Give the preparation type.
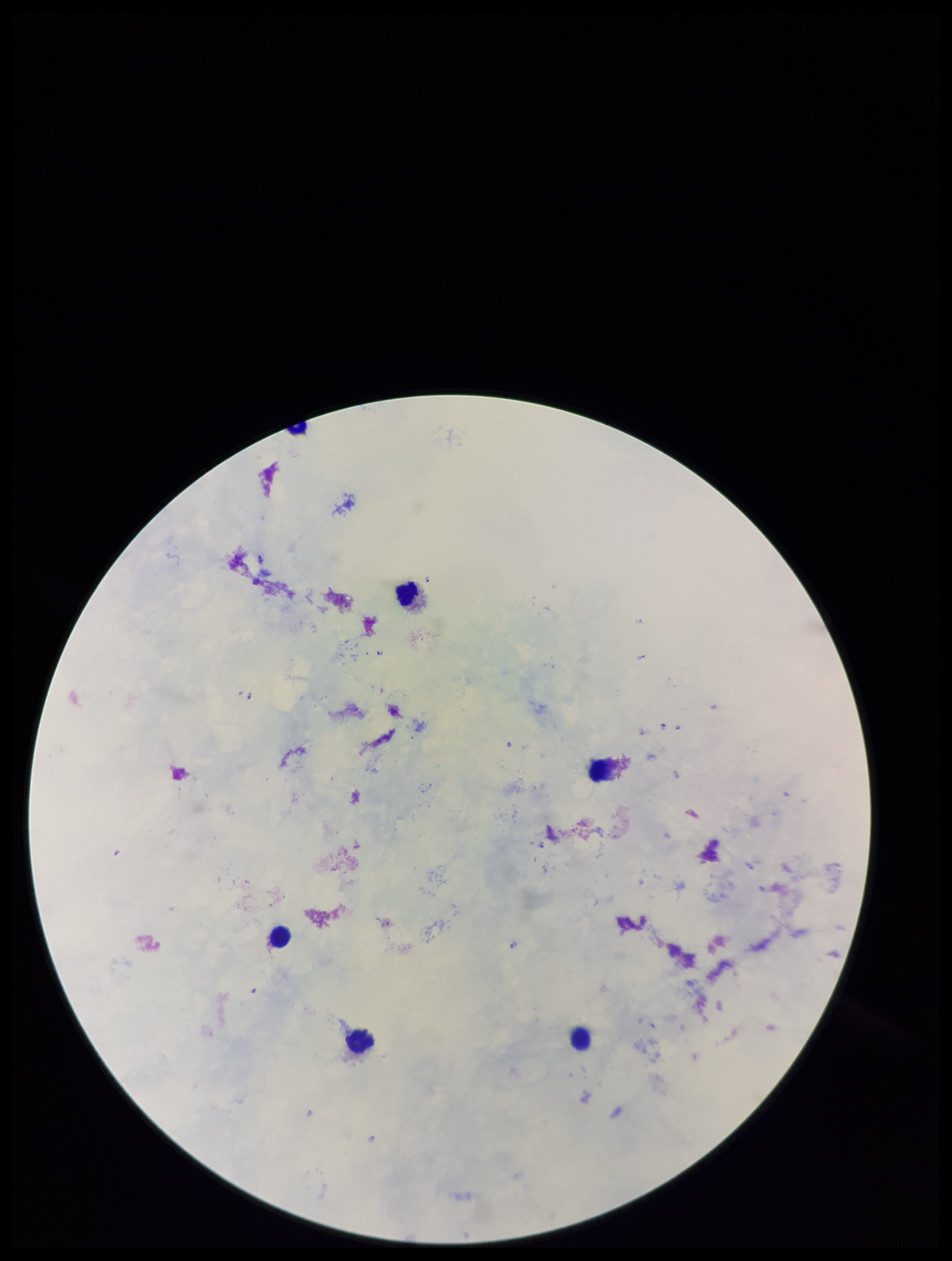
A thick smear.

field_of_view: single
capture: smartphone photograph through the microscope eyepiece
stain: Giemsa
plasmodium_parasites: seen
species_reported_for_this_patient: Plasmodium falciparum
patient_malaria_status: infected
leukocyte_count: 5
parasite_count: 8
image_size: 952×1261 pixels